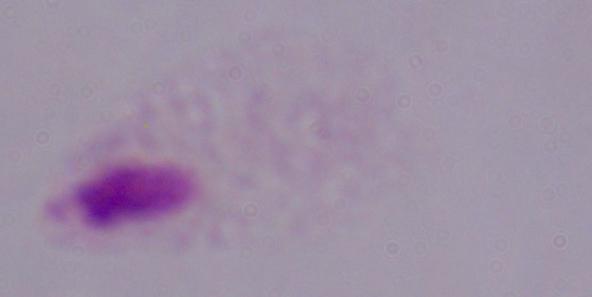
identification = trichomonad
magnification = 1000x
modality = micrograph